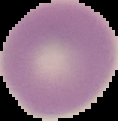
image type = segmented cell region with the area outside set to black
image size = 118×121 pixels
preparation = thin blood film
result = no Plasmodium parasites detected